Name the cell type shown.
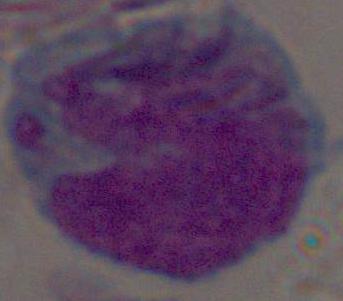

This is a leukocyte.

Summary:
  - Magnification: 1000x
  - Modality: micrograph